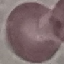
Result: no malaria parasites seen. Automatically extracted cell patch, resized to 64 × 64 pixels. Thin smear of blood. Photographed with a smartphone camera at the microscope eyepiece. Giemsa stain.